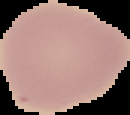
image size = 130×115 pixels
result = negative for malaria parasites
image type = segmented cell region with the area outside set to black
preparation = thin blood film